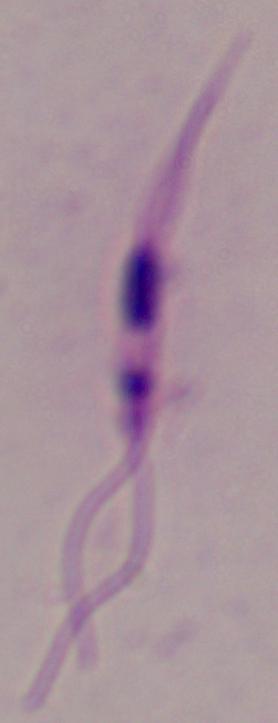
A Leishmania parasite is seen. Captured at 1000x magnification. Micrograph.